Assess this cell for malaria.
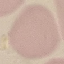
It is uninfected.

Summary:
  - Preparation: thin blood film
  - Capture: smartphone through the microscope eyepiece
  - Stain: Giemsa
  - Image type: automatically extracted cell patch, resized to 64 × 64 pixels